Name the parasite shown.
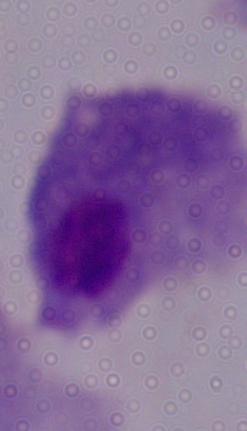

This is a trichomonad.

Captured at 1000x magnification. Micrograph.